Assess this cell for malaria.
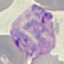

It is parasitized.

stain = Giemsa
preparation = thin blood smear
capture = smartphone camera at the microscope eyepiece
image type = automatically extracted cell patch, resized to 64 × 64 pixels